Point out each Plasmodium parasite.
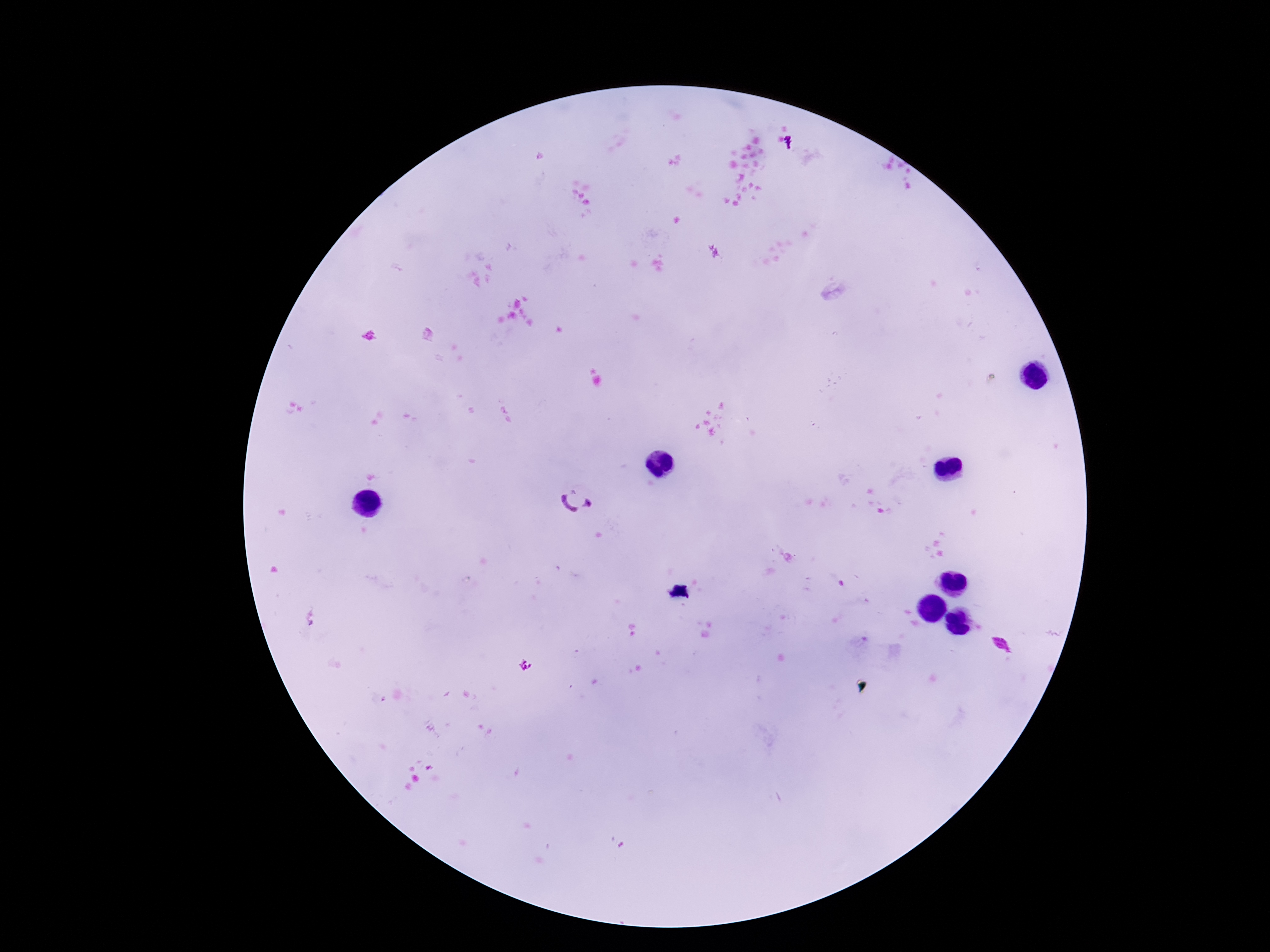
Approximate centers as [x, y] in pixels.
Plasmodium parasites: [575, 502], [312, 617], [524, 665].

Summary:
  - Patient malaria status: infected
  - Stain: Giemsa
  - Magnification: 100x
  - Capture: smartphone camera through the microscope eyepiece
  - Preparation: thick blood film
  - Field of view: one from this slide
  - Image size: 1270×952 pixels